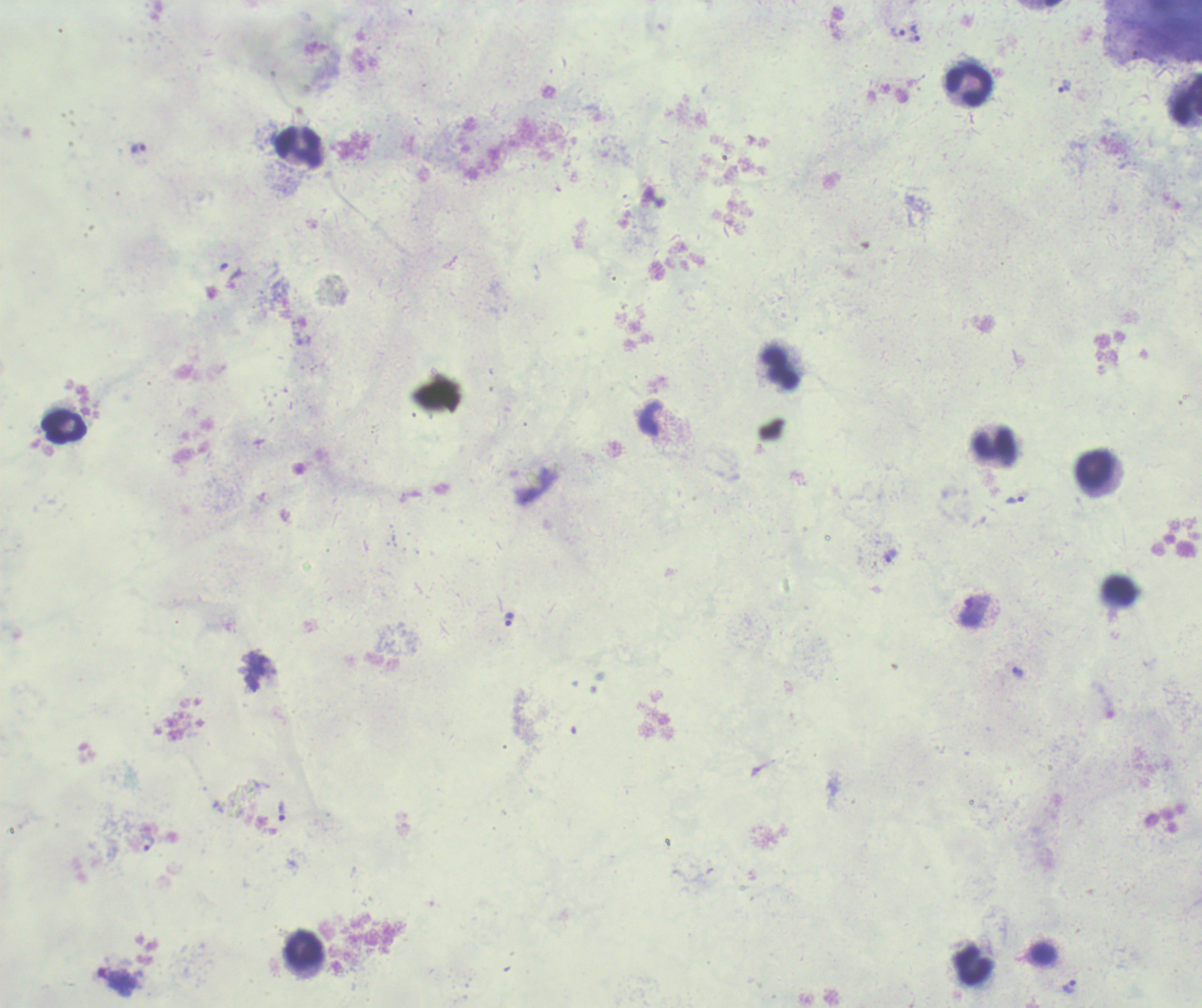
Approximate centers as {x, y} in pixels. Trophozoite locations: {897, 32}, {915, 33}, {1064, 86}, {138, 149}, {1015, 499}, {890, 556}, {974, 609}, {509, 620}, {1018, 673}, {281, 811}, {149, 844}, {1069, 987}. Leukocyte locations: {968, 84}, {1185, 99}, {299, 148}, {779, 368}, {65, 427}, {994, 445}, {1092, 469}, {1120, 592}, {303, 948}, {1042, 954}, {972, 964}. Background quality: poor. Image is 1202×1008 pixels. Single field of view. Thick smear of blood. Result: positive for malaria parasites. Romanowsky stain. Captured at 100x magnification. Previously used in a real diagnosis.